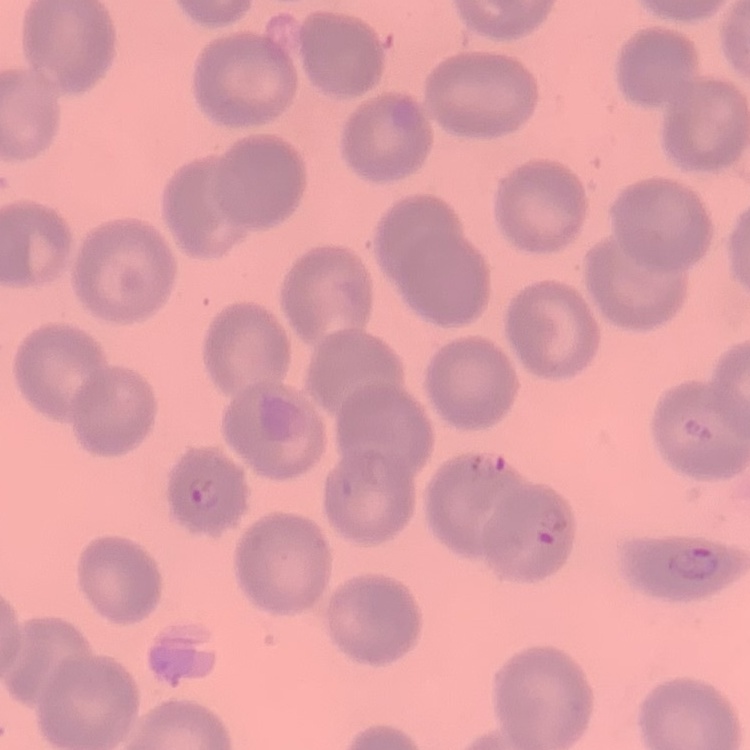 The erythrocytes show no rouleaux formation. Thin blood smear. One tile cut from a larger photomicrograph. Stained with either Field's or Giemsa.